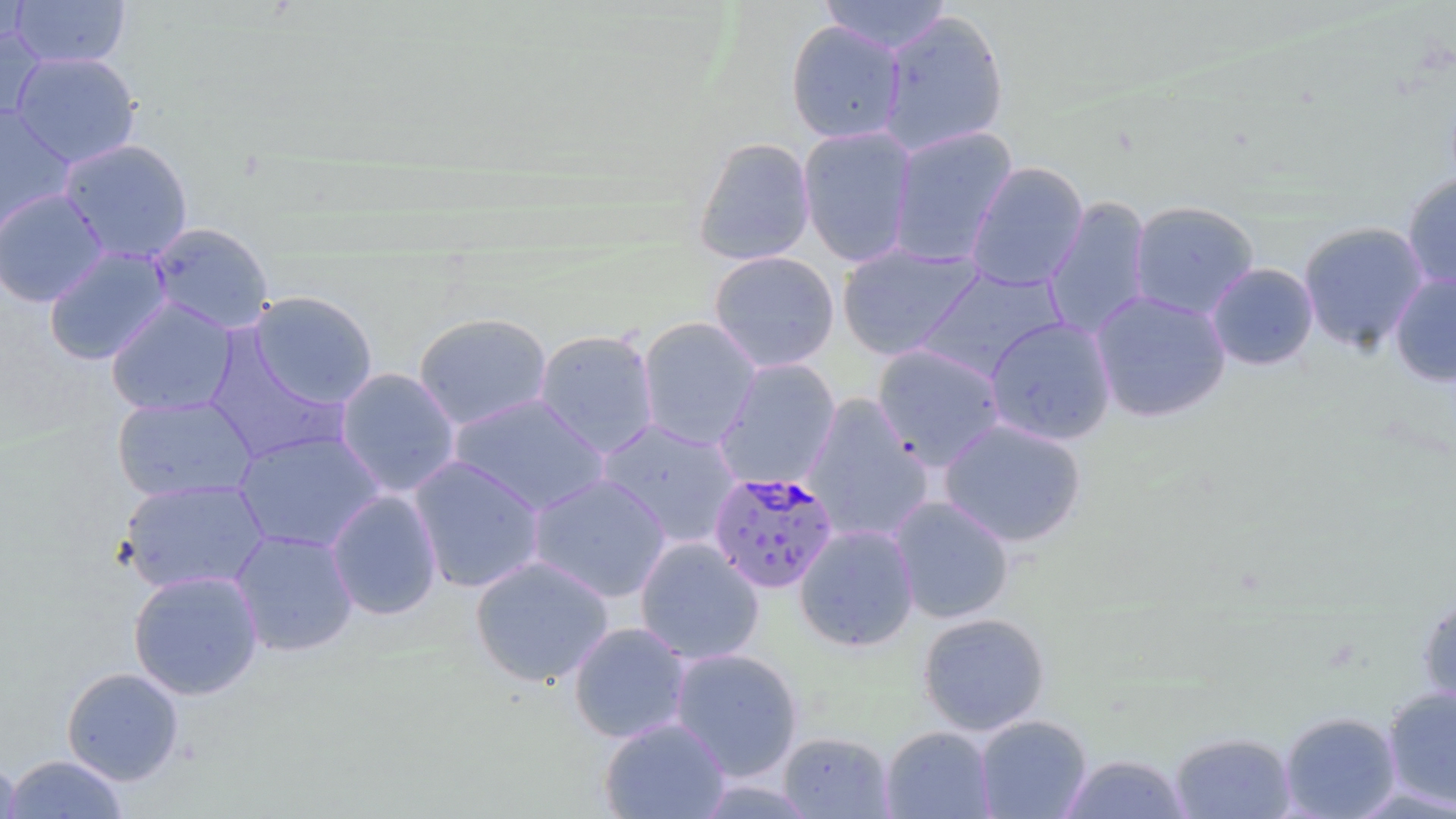

{
  "slide_level_diagnosis": "Plasmodium falciparum",
  "uninfected_red_blood_cell_locations": "approximate bounding boxes as [x1, y1, x2, y2] in pixels: [0, 0, 30, 54], [10, 0, 130, 68], [818, 0, 953, 54], [878, 10, 1010, 156], [785, 20, 906, 144], [0, 26, 46, 129], [11, 51, 141, 168], [0, 104, 75, 236], [798, 125, 917, 268], [887, 126, 1017, 267], [693, 137, 816, 266], [58, 138, 194, 264], [965, 160, 1088, 292], [1401, 173, 1456, 293], [0, 188, 110, 307], [1043, 195, 1153, 341], [1128, 200, 1259, 320], [1297, 221, 1430, 354], [146, 222, 275, 335], [837, 243, 982, 361], [44, 247, 173, 365], [708, 250, 840, 373], [1206, 262, 1319, 370], [915, 267, 1066, 380], [1389, 273, 1456, 386], [1089, 290, 1231, 423], [248, 291, 379, 409], [106, 297, 239, 416], [413, 312, 553, 430], [637, 316, 762, 450], [984, 317, 1117, 445], [533, 328, 660, 458], [203, 336, 349, 464], [872, 343, 1007, 471], [713, 358, 840, 491], [335, 367, 461, 498], [448, 393, 611, 516], [800, 394, 934, 545], [112, 395, 259, 502], [595, 418, 742, 549], [938, 418, 1087, 548], [233, 430, 386, 554], [408, 454, 546, 593], [527, 473, 672, 604], [118, 478, 271, 595], [325, 489, 443, 620], [889, 496, 1014, 624], [794, 523, 920, 652], [229, 528, 359, 657], [634, 537, 764, 665], [470, 555, 614, 688], [128, 569, 264, 700], [1417, 592, 1456, 713], [917, 612, 1051, 735], [568, 622, 691, 744], [669, 648, 803, 781], [61, 666, 185, 786], [1382, 686, 1456, 811], [1279, 711, 1402, 818], [975, 714, 1092, 818], [598, 717, 731, 818], [880, 725, 997, 818], [1169, 731, 1296, 818], [779, 732, 894, 817], [3, 754, 130, 818], [1059, 754, 1195, 818], [0, 755, 21, 819]",
  "plasmodium_falciparum_infected_red_blood_cell_locations": "approximate bounding boxes as [x1, y1, x2, y2] in pixels: [708, 471, 839, 594]",
  "preparation": "thin blood film",
  "stain": "May-Grünwald-Giemsa",
  "modality": "light microscopy",
  "image_size": "1456×819 pixels",
  "field_of_view": "single",
  "magnification": "1000x"
}